Outline each blood parasite and name the species.
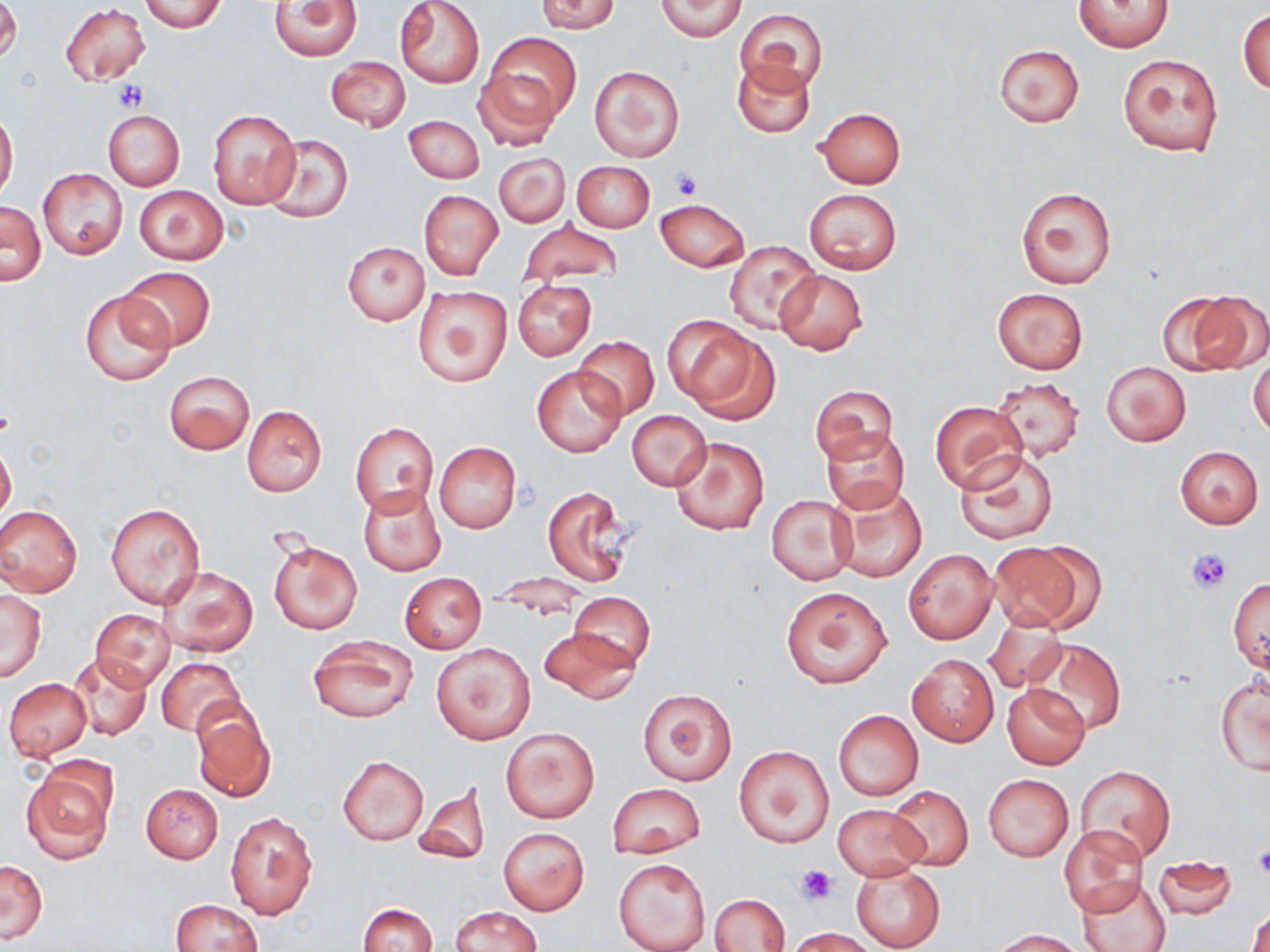
No blood parasites observed.

slide_level_diagnosis: no evidence of blood parasites
image_size: 1270×952 pixels
magnification: 1000x
uninfected_red_blood_cell_locations: 'approximate bounding boxes as (x1,y1)-(x2,y2) corner pairs in pixels: (0,0)-(21,64), (140,0)-(227,33), (269,0)-(363,60), (393,0)-(486,88), (533,0)-(622,32), (656,0)-(746,40), (1075,1)-(1173,52), (59,4)-(151,85), (736,8)-(826,92), (1238,8)-(1269,94), (483,29)-(581,132), (993,43)-(1085,128), (1116,53)-(1224,158), (327,57)-(410,130), (731,57)-(816,137), (590,65)-(684,162), (473,68)-(562,153), (814,107)-(905,188), (103,109)-(184,190), (207,109)-(300,208), (0,111)-(18,201), (404,114)-(485,183), (262,133)-(353,223), (494,153)-(569,228), (571,160)-(655,232), (38,168)-(128,260), (133,186)-(228,263), (1015,187)-(1115,290), (803,188)-(902,275), (418,189)-(503,279), (656,198)-(749,271), (0,202)-(45,286), (519,219)-(622,284), (725,241)-(819,333), (343,242)-(429,324), (116,266)-(215,352), (774,269)-(868,357), (512,280)-(596,360), (413,287)-(512,387), (992,287)-(1088,373), (80,291)-(174,387), (1175,291)-(1270,373), (666,317)-(777,422), (574,337)-(659,420), (1249,350)-(1270,439), (1101,361)-(1191,446), (532,365)-(627,457), (163,370)-(254,454), (992,377)-(1084,460), (810,384)-(899,465), (929,402)-(1026,494), (242,405)-(327,496), (627,410)-(711,491), (351,421)-(439,516), (819,427)-(911,515), (670,435)-(770,536), (434,441)-(521,532), (0,444)-(16,528), (1175,445)-(1264,528), (957,450)-(1060,545), (358,484)-(446,576), (831,484)-(927,583), (540,486)-(635,588), (766,495)-(856,583), (106,502)-(204,608), (0,504)-(82,597), (268,538)-(362,635), (986,541)-(1098,633), (903,549)-(998,645), (155,566)-(257,657), (398,572)-(486,655), (1229,577)-(1269,673), (779,585)-(892,689), (1,589)-(47,682), (569,593)-(655,670), (90,609)-(176,691), (982,615)-(1067,693), (539,627)-(638,704), (308,634)-(418,724), (1031,639)-(1126,735), (432,642)-(535,745), (68,653)-(152,740), (908,654)-(999,746), (154,657)-(245,738), (1215,675)-(1269,776), (4,678)-(91,759), (1002,683)-(1091,770), (637,688)-(737,785), (191,704)-(277,802), (832,710)-(923,801), (501,727)-(600,822), (734,745)-(834,848), (337,755)-(428,846), (1076,764)-(1174,863), (22,765)-(114,861), (983,774)-(1073,861), (607,783)-(706,858), (140,784)-(223,863), (414,784)-(491,866), (887,785)-(974,869), (832,804)-(927,880), (225,810)-(320,919), (1059,826)-(1149,915), (498,828)-(589,915), (1151,856)-(1238,920), (613,857)-(711,952), (1,858)-(48,943), (850,864)-(946,952), (1077,876)-(1171,952), (711,893)-(789,951), (1247,896)-(1269,952), (170,899)-(263,951), (357,902)-(439,952), (449,905)-(543,952), (785,927)-(880,952), (991,929)-(1086,951)'
stain: May-Grünwald-Giemsa
modality: optical microscopy
field_of_view: single
platelet_locations: 'approximate bounding boxes as (x1,y1)-(x2,y2) corner pairs in pixels: (114,82)-(147,111), (671,168)-(702,201), (1187,547)-(1231,592), (1251,846)-(1270,879), (795,865)-(838,905)'
preparation: thin blood film